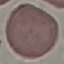
result = no malaria parasites seen
image type = automatically extracted cell patch, resized to 64 × 64 pixels
capture = smartphone through the microscope eyepiece
preparation = thin smear
stain = Giemsa